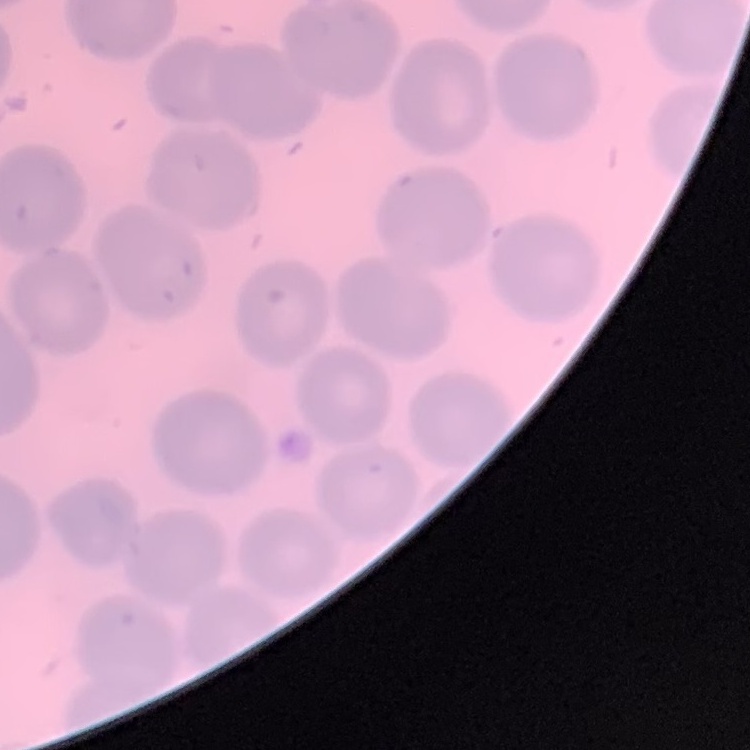 The erythrocytes exhibit no rouleaux formation. Stained with either Field's or Giemsa. Thin blood film. Square crop of a larger photomicrograph.